State the blood parasite species.
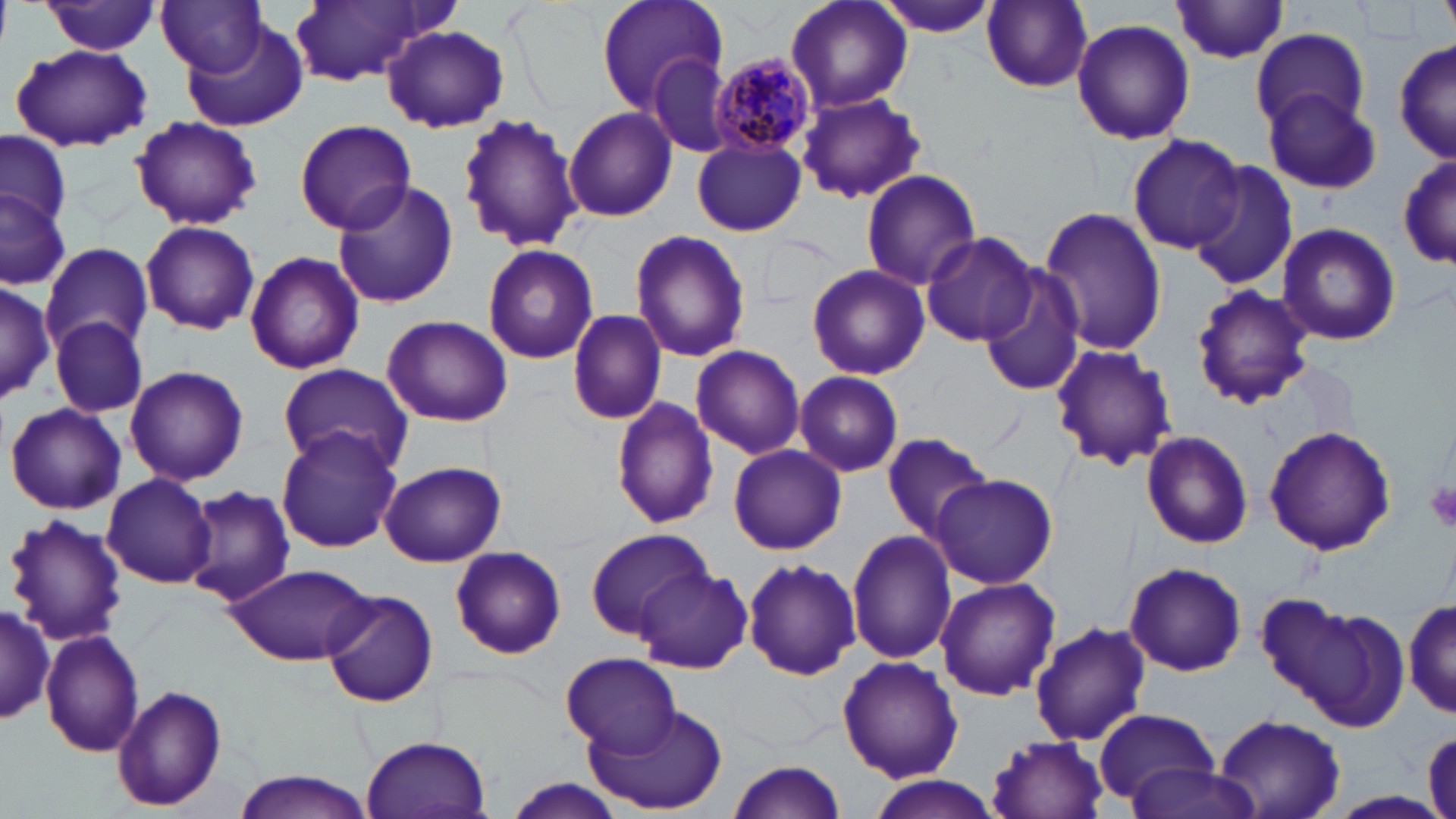

Plasmodium malariae.

Summary:
  - Coordinate format: approximate bounding boxes as named x1/y1/x2/y2 corners in pixels
  - Uninfected red blood cell locations: (x1=287, y1=0, x2=444, y2=87), (x1=594, y1=0, x2=728, y2=111), (x1=785, y1=0, x2=913, y2=113), (x1=43, y1=1, x2=162, y2=55), (x1=158, y1=1, x2=268, y2=74), (x1=982, y1=1, x2=1094, y2=91), (x1=876, y1=2, x2=999, y2=39), (x1=1170, y1=2, x2=1290, y2=65), (x1=1071, y1=20, x2=1195, y2=145), (x1=382, y1=24, x2=509, y2=133), (x1=184, y1=26, x2=307, y2=133), (x1=1251, y1=28, x2=1370, y2=133), (x1=1393, y1=36, x2=1453, y2=163), (x1=10, y1=44, x2=153, y2=151), (x1=645, y1=52, x2=739, y2=158), (x1=1259, y1=85, x2=1382, y2=195), (x1=797, y1=93, x2=925, y2=205), (x1=563, y1=106, x2=678, y2=222), (x1=457, y1=113, x2=584, y2=253), (x1=129, y1=116, x2=262, y2=230), (x1=293, y1=119, x2=418, y2=233), (x1=1, y1=129, x2=73, y2=231), (x1=1129, y1=134, x2=1246, y2=253), (x1=691, y1=140, x2=806, y2=236), (x1=1395, y1=149, x2=1452, y2=271), (x1=1189, y1=161, x2=1301, y2=292), (x1=859, y1=169, x2=983, y2=288), (x1=329, y1=176, x2=460, y2=308), (x1=0, y1=183, x2=71, y2=294), (x1=1037, y1=206, x2=1168, y2=357), (x1=140, y1=219, x2=260, y2=335), (x1=1276, y1=223, x2=1402, y2=347), (x1=628, y1=230, x2=752, y2=363), (x1=918, y1=232, x2=1038, y2=347), (x1=483, y1=243, x2=598, y2=366), (x1=42, y1=245, x2=153, y2=356), (x1=243, y1=250, x2=365, y2=376), (x1=806, y1=263, x2=929, y2=380), (x1=976, y1=266, x2=1087, y2=397), (x1=0, y1=274, x2=54, y2=405), (x1=1189, y1=285, x2=1313, y2=408), (x1=569, y1=308, x2=665, y2=424), (x1=380, y1=315, x2=513, y2=428), (x1=51, y1=316, x2=148, y2=418), (x1=690, y1=344, x2=806, y2=461), (x1=1049, y1=344, x2=1177, y2=471), (x1=275, y1=363, x2=413, y2=478), (x1=123, y1=365, x2=249, y2=486), (x1=794, y1=370, x2=903, y2=477), (x1=609, y1=396, x2=723, y2=530), (x1=5, y1=401, x2=126, y2=515), (x1=275, y1=425, x2=401, y2=552), (x1=1263, y1=426, x2=1396, y2=554), (x1=880, y1=430, x2=994, y2=541), (x1=1142, y1=431, x2=1255, y2=547), (x1=727, y1=444, x2=845, y2=556), (x1=379, y1=460, x2=507, y2=567), (x1=930, y1=472, x2=1058, y2=588), (x1=102, y1=473, x2=219, y2=587), (x1=183, y1=484, x2=297, y2=608), (x1=4, y1=513, x2=129, y2=645), (x1=584, y1=526, x2=713, y2=639), (x1=846, y1=529, x2=957, y2=666), (x1=448, y1=545, x2=567, y2=660), (x1=742, y1=557, x2=861, y2=681), (x1=1124, y1=560, x2=1247, y2=677), (x1=225, y1=563, x2=372, y2=665), (x1=633, y1=566, x2=753, y2=672), (x1=934, y1=576, x2=1059, y2=700), (x1=321, y1=589, x2=439, y2=708), (x1=1405, y1=595, x2=1456, y2=717), (x1=1270, y1=597, x2=1410, y2=728), (x1=0, y1=602, x2=53, y2=728), (x1=1029, y1=621, x2=1152, y2=745), (x1=41, y1=630, x2=145, y2=757), (x1=557, y1=651, x2=681, y2=756), (x1=837, y1=655, x2=963, y2=783), (x1=112, y1=684, x2=228, y2=812), (x1=584, y1=703, x2=729, y2=814), (x1=1092, y1=707, x2=1221, y2=807), (x1=1214, y1=713, x2=1346, y2=819), (x1=1422, y1=729, x2=1456, y2=818), (x1=360, y1=733, x2=492, y2=819), (x1=983, y1=733, x2=1111, y2=819), (x1=725, y1=759, x2=846, y2=819), (x1=1122, y1=760, x2=1262, y2=819), (x1=231, y1=770, x2=374, y2=819), (x1=862, y1=776, x2=1006, y2=819), (x1=499, y1=777, x2=629, y2=819), (x1=1331, y1=790, x2=1452, y2=818)
  - Plasmodium malariae-infected red blood cell locations: (x1=712, y1=53, x2=819, y2=158)
  - Platelet locations: (x1=1425, y1=481, x2=1456, y2=532)
  - Modality: optical microscopy
  - Stain: May-Grünwald-Giemsa
  - Image size: 1456×819 pixels
  - Preparation: thin blood smear
  - Magnification: 1000x
  - Field of view: one of a larger specimen